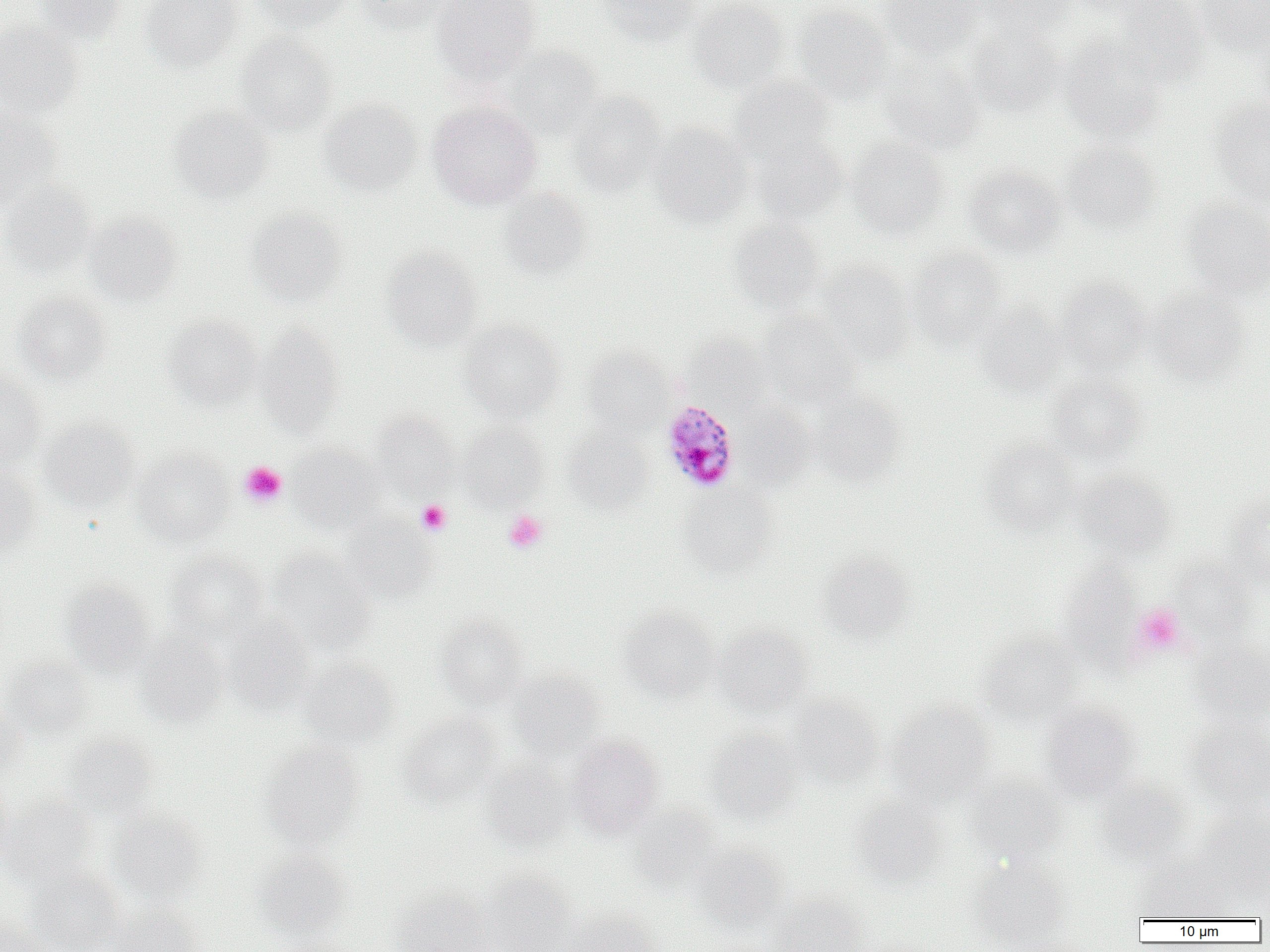
Approximate bounding boxes as (x1,y1)-(x2,y2) corner pairs in pixels. Uninfected red blood cell locations: (35,0)-(127,44), (139,0)-(245,72), (250,0)-(352,33), (354,0)-(452,34), (430,0)-(541,82), (597,0)-(699,45), (688,0)-(789,93), (878,0)-(986,59), (980,0)-(1076,43), (1113,0)-(1211,88), (1197,0)-(1270,58), (792,5)-(894,105), (0,21)-(82,120), (1254,24)-(1270,114), (966,26)-(1065,117), (235,32)-(336,135), (1060,37)-(1168,142), (504,45)-(603,139), (878,56)-(985,154), (728,76)-(835,163), (568,91)-(667,197), (1209,94)-(1270,206), (319,99)-(422,196), (428,101)-(542,209), (169,105)-(275,202), (0,107)-(62,207), (648,123)-(752,227), (749,134)-(847,224), (846,137)-(950,240), (1060,140)-(1162,235), (962,165)-(1067,258), (0,181)-(96,280), (499,188)-(592,281), (1180,197)-(1270,298), (245,208)-(346,308), (84,210)-(182,306), (728,218)-(825,313), (381,247)-(483,351), (906,247)-(1008,349), (819,262)-(915,362), (1056,277)-(1152,373), (1146,286)-(1252,387), (13,291)-(112,384), (974,299)-(1069,398), (758,312)-(863,409), (163,314)-(263,410), (459,320)-(565,422), (256,325)-(345,434), (683,334)-(773,411), (580,347)-(675,435), (0,372)-(46,468), (1044,374)-(1148,468), (811,391)-(905,486), (735,404)-(816,489), (371,410)-(458,496), (38,417)-(140,512), (458,422)-(547,510), (564,427)-(656,513), (978,439)-(1079,533), (287,444)-(390,535), (132,449)-(235,546), (0,466)-(40,558), (1071,470)-(1177,561), (679,486)-(779,578), (1224,490)-(1270,587), (342,517)-(437,603), (268,548)-(376,652), (166,550)-(267,642), (818,551)-(916,643), (1168,558)-(1257,643), (1058,560)-(1142,665), (61,579)-(156,678), (618,607)-(720,702), (436,613)-(530,708), (224,615)-(314,715), (714,624)-(814,716), (977,632)-(1086,727), (135,634)-(229,728), (1189,638)-(1270,728), (2,658)-(95,741), (300,658)-(399,749), (507,671)-(605,757), (787,694)-(883,788), (0,697)-(26,779), (885,701)-(995,807), (1040,702)-(1140,801), (400,712)-(501,804), (1185,720)-(1270,810), (703,728)-(804,824), (64,733)-(156,817), (567,735)-(664,837), (261,741)-(364,848), (480,758)-(574,850), (965,773)-(1068,866), (0,776)-(14,862), (1095,780)-(1192,867), (849,794)-(949,889), (2,795)-(98,887), (629,804)-(724,893), (1196,805)-(1270,896), (108,810)-(207,903), (691,844)-(789,932), (251,850)-(351,943), (1138,851)-(1231,921), (969,862)-(1071,949), (27,865)-(126,952), (481,873)-(579,952), (390,887)-(494,952), (770,896)-(869,952), (109,905)-(208,952), (563,906)-(663,952), (0,913)-(46,952). Platelet locations: (239,461)-(287,507), (416,499)-(451,535), (503,510)-(548,553), (1133,604)-(1187,656). Plasmodium malariae-infected red blood cell locations: (661,400)-(740,492). Slide-level diagnosis: Plasmodium malariae. Captured at 1000x magnification. Single field of view. Image is 1270×952 pixels. Light microscopy. Thin blood film.